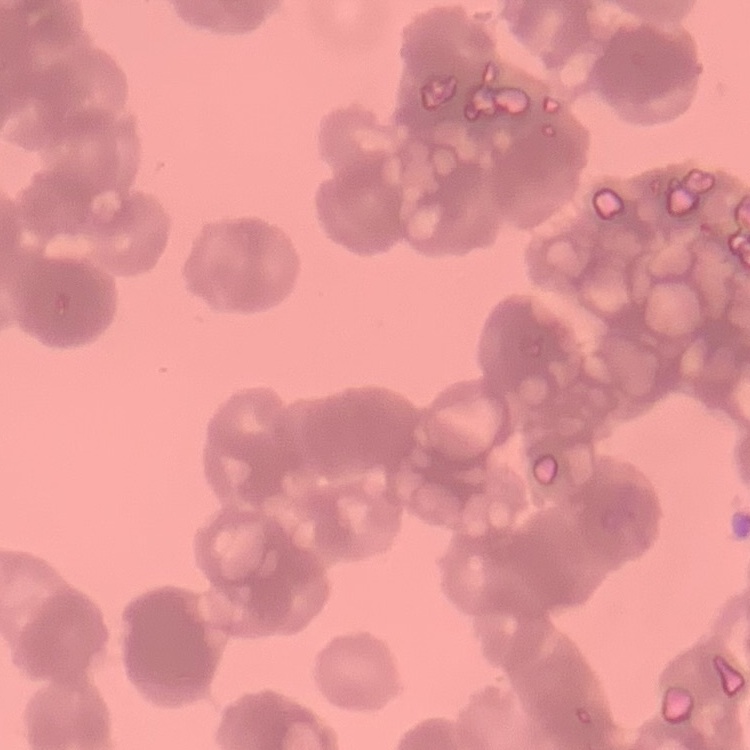
Summary:
  - Red blood cell morphology: rouleaux formation
  - Preparation: thin blood film
  - Image type: one tile cut from a larger photomicrograph
  - Stain: Field's or Giemsa